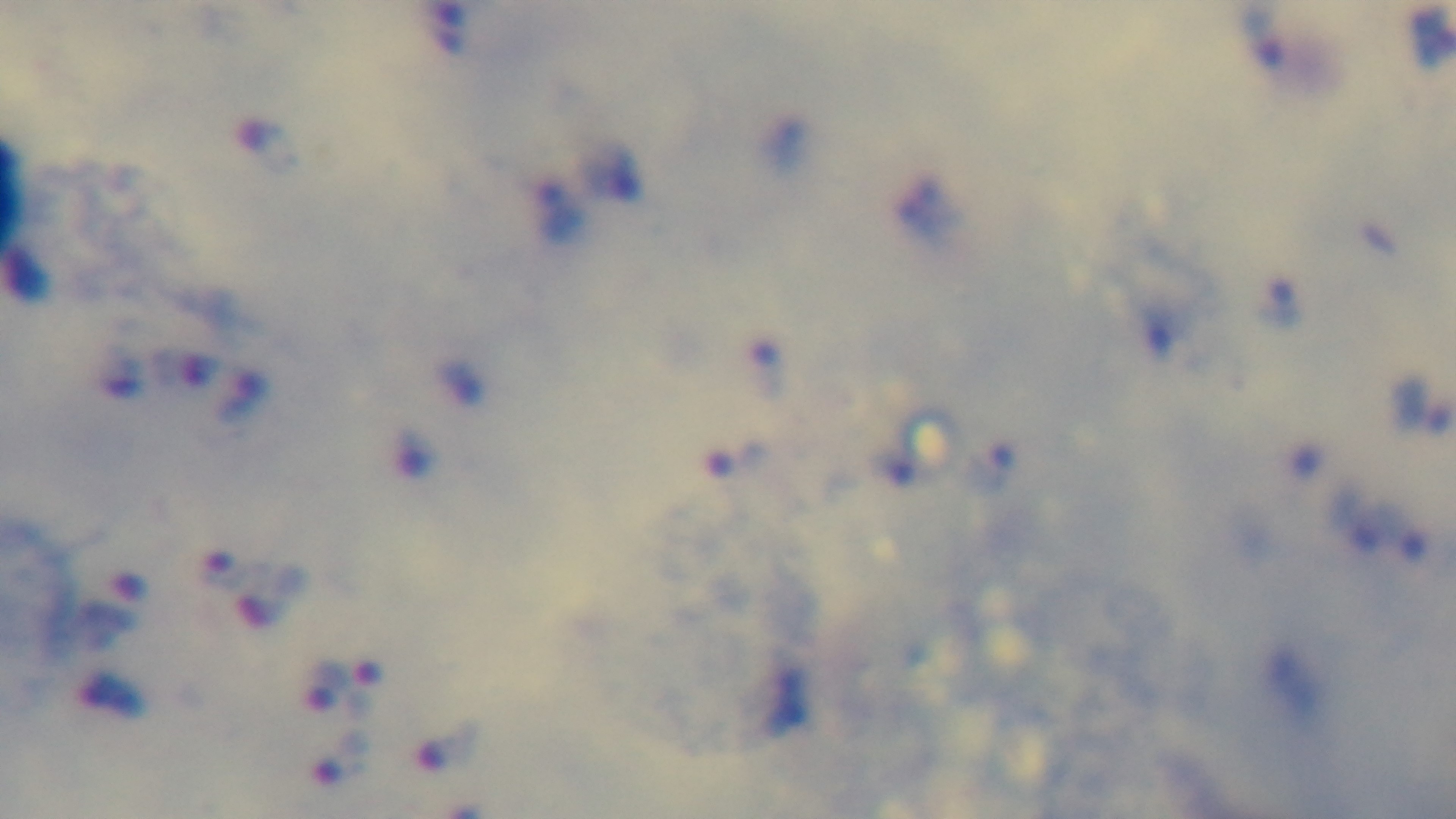
Giemsa-stained. Preparation: thick. Malaria status: infected. 100x oil-immersion objective. Mounted 4K digital camera. Light microscopy. One field from the slide.